Name the parasite shown.
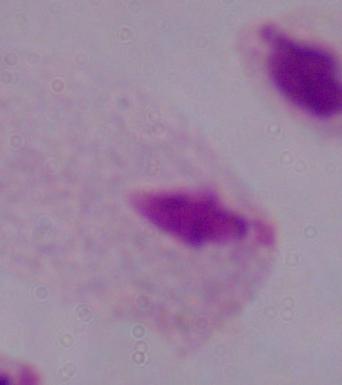
A trichomonad.

{
  "modality": "photomicrograph",
  "magnification": "1000x"
}